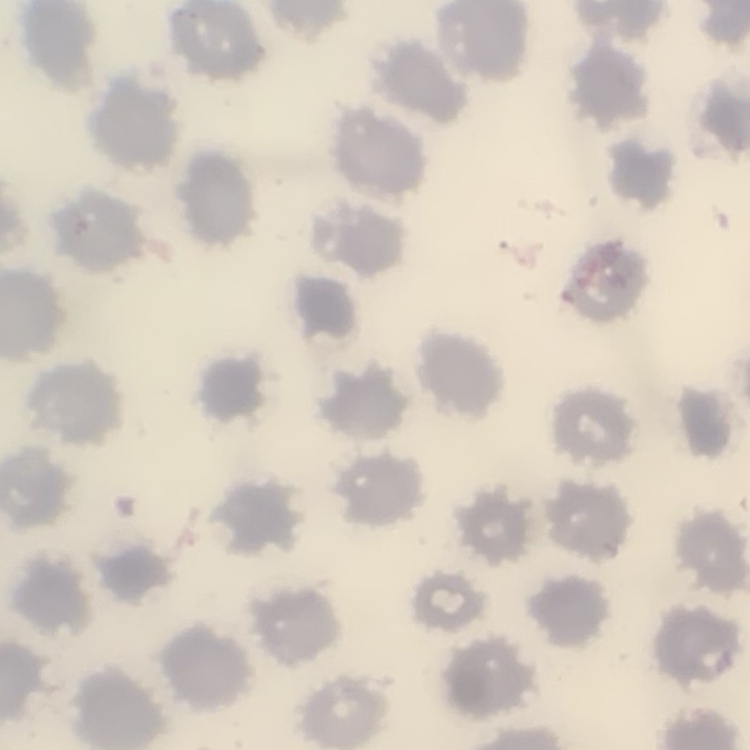
erythrocyte_morphology: no rouleaux formation
preparation: thin peripheral smear
image_type: one tile cut from a larger photomicrograph
stain: Field's or Giemsa